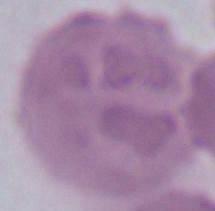
{
  "magnification": "1000x",
  "modality": "photomicrograph",
  "identification": "red blood cell"
}